Give the position of every malaria parasite.
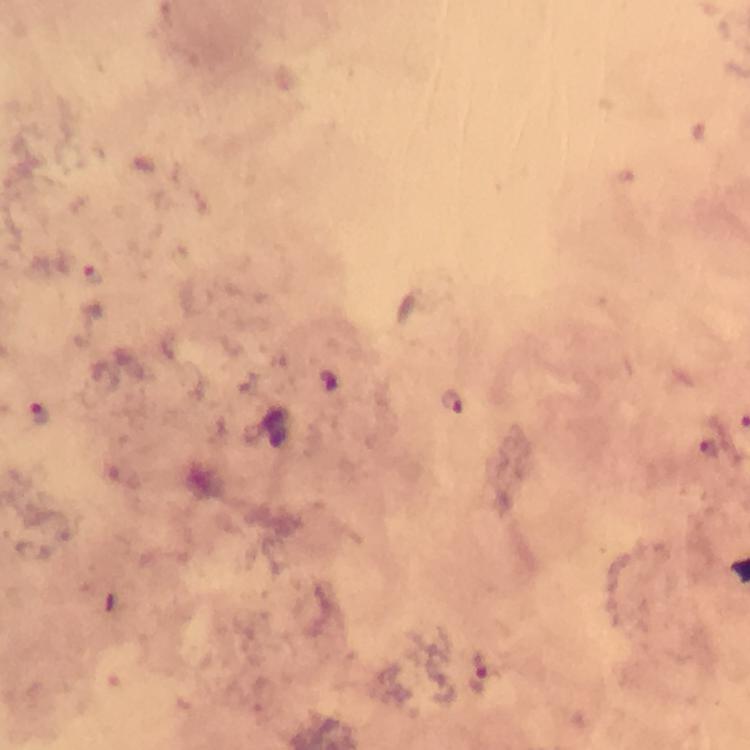

Approximate centers as [x, y] in pixels.
Malaria parasites: [91, 274], [454, 400], [38, 411], [479, 674].

Summary:
  - Stain: Giemsa
  - Immersion oil: used
  - Image size: 750×750 pixels
  - Context: from a malaria diagnostic workup
  - Preparation: thick blood smear
  - Magnification: 100x
  - Capture: smartphone camera through the microscope
  - Cropped from: one field of view